Name the parasite shown.
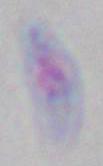

Toxoplasma gondii.

Micrograph. 1000x magnification.